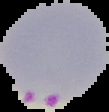

The area outside the segmented cell region is set to black. From a thin blood film. Image is 109×112 pixels. Result: Plasmodium parasites detected.